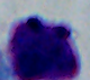
Captured at 1000x magnification. Photomicrograph. A white blood cell is seen.